Locate and identify every blood parasite.
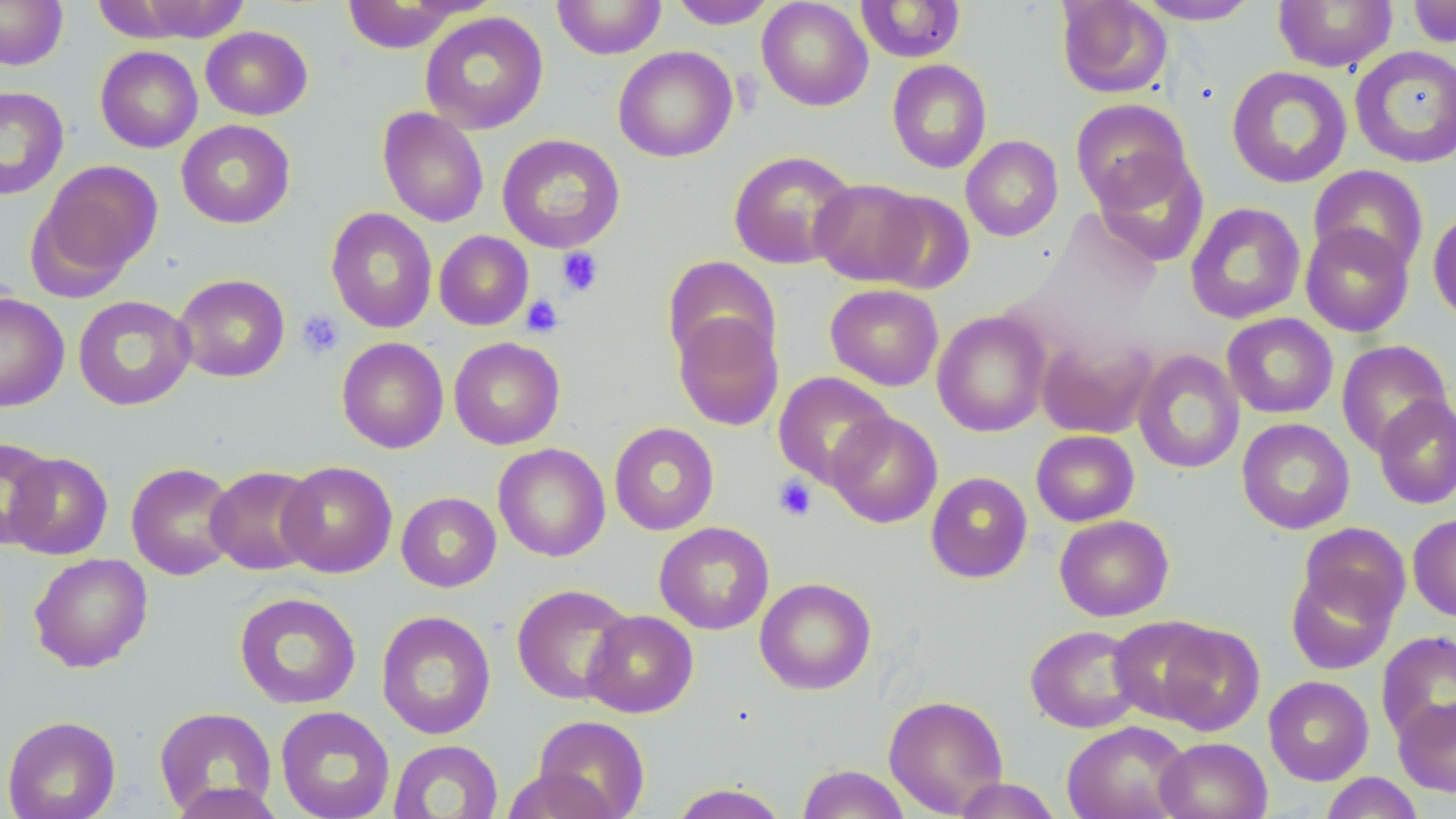
No blood parasites seen.

Summary:
  - Coordinate format: approximate bounding boxes as named x1/y1/x2/y2 corners in pixels
  - Platelet locations: (x1=556, y1=247, x2=604, y2=297), (x1=521, y1=295, x2=564, y2=338), (x1=296, y1=309, x2=345, y2=360), (x1=773, y1=474, x2=818, y2=522)
  - Uninfected red blood cell locations: (x1=0, y1=0, x2=68, y2=70), (x1=552, y1=0, x2=666, y2=59), (x1=756, y1=0, x2=873, y2=111), (x1=1055, y1=0, x2=1172, y2=99), (x1=1133, y1=0, x2=1262, y2=25), (x1=1273, y1=0, x2=1398, y2=73), (x1=121, y1=1, x2=253, y2=42), (x1=342, y1=1, x2=464, y2=53), (x1=669, y1=1, x2=778, y2=29), (x1=855, y1=1, x2=966, y2=62), (x1=1407, y1=1, x2=1456, y2=48), (x1=420, y1=12, x2=549, y2=134), (x1=200, y1=26, x2=313, y2=120), (x1=1350, y1=45, x2=1456, y2=168), (x1=95, y1=46, x2=203, y2=153), (x1=613, y1=46, x2=737, y2=162), (x1=887, y1=59, x2=992, y2=173), (x1=1226, y1=66, x2=1353, y2=188), (x1=0, y1=86, x2=69, y2=199), (x1=1070, y1=97, x2=1192, y2=210), (x1=378, y1=107, x2=489, y2=227), (x1=176, y1=119, x2=295, y2=229), (x1=497, y1=133, x2=625, y2=253), (x1=961, y1=135, x2=1063, y2=241), (x1=728, y1=150, x2=857, y2=269), (x1=1094, y1=151, x2=1209, y2=267), (x1=31, y1=160, x2=164, y2=292), (x1=1309, y1=164, x2=1429, y2=275), (x1=810, y1=178, x2=928, y2=286), (x1=870, y1=190, x2=975, y2=294), (x1=1185, y1=202, x2=1306, y2=324), (x1=325, y1=207, x2=438, y2=334), (x1=1427, y1=207, x2=1456, y2=326), (x1=1300, y1=223, x2=1414, y2=337), (x1=434, y1=231, x2=534, y2=330), (x1=662, y1=256, x2=782, y2=369), (x1=173, y1=274, x2=290, y2=382), (x1=825, y1=284, x2=944, y2=391), (x1=0, y1=293, x2=69, y2=412), (x1=73, y1=295, x2=196, y2=411), (x1=672, y1=310, x2=784, y2=431), (x1=932, y1=310, x2=1051, y2=437), (x1=1222, y1=313, x2=1338, y2=418), (x1=1036, y1=335, x2=1159, y2=439), (x1=336, y1=337, x2=449, y2=454), (x1=449, y1=337, x2=565, y2=450), (x1=1336, y1=340, x2=1453, y2=456), (x1=1133, y1=350, x2=1245, y2=474), (x1=773, y1=371, x2=895, y2=488), (x1=1372, y1=394, x2=1456, y2=509), (x1=826, y1=412, x2=942, y2=528), (x1=1236, y1=417, x2=1355, y2=534), (x1=609, y1=422, x2=720, y2=535), (x1=1031, y1=430, x2=1139, y2=527), (x1=0, y1=436, x2=57, y2=551), (x1=493, y1=443, x2=610, y2=562), (x1=4, y1=452, x2=113, y2=560), (x1=277, y1=460, x2=397, y2=578), (x1=126, y1=462, x2=240, y2=580), (x1=205, y1=465, x2=321, y2=575), (x1=925, y1=471, x2=1032, y2=583), (x1=396, y1=492, x2=501, y2=592), (x1=1408, y1=512, x2=1456, y2=622), (x1=1055, y1=514, x2=1174, y2=621), (x1=654, y1=521, x2=774, y2=635), (x1=1297, y1=522, x2=1411, y2=628), (x1=29, y1=553, x2=153, y2=672), (x1=1285, y1=563, x2=1398, y2=674), (x1=754, y1=577, x2=876, y2=695), (x1=511, y1=583, x2=635, y2=704), (x1=234, y1=592, x2=362, y2=709), (x1=582, y1=609, x2=698, y2=717), (x1=376, y1=610, x2=496, y2=739), (x1=1108, y1=615, x2=1227, y2=724), (x1=1152, y1=622, x2=1265, y2=736), (x1=1025, y1=625, x2=1146, y2=733), (x1=1376, y1=631, x2=1456, y2=746), (x1=1263, y1=675, x2=1374, y2=785), (x1=883, y1=694, x2=1009, y2=817), (x1=1393, y1=696, x2=1456, y2=796), (x1=275, y1=705, x2=395, y2=819), (x1=153, y1=706, x2=277, y2=816), (x1=2, y1=715, x2=121, y2=819), (x1=531, y1=715, x2=651, y2=819), (x1=1061, y1=721, x2=1192, y2=819), (x1=1154, y1=736, x2=1272, y2=819), (x1=388, y1=740, x2=504, y2=819), (x1=797, y1=764, x2=911, y2=819), (x1=501, y1=765, x2=619, y2=819), (x1=1320, y1=772, x2=1424, y2=819), (x1=952, y1=777, x2=1063, y2=818), (x1=164, y1=782, x2=286, y2=819), (x1=669, y1=782, x2=789, y2=819)
  - Slide-level diagnosis: negative for blood parasites
  - Stain: May-Grünwald-Giemsa
  - Modality: optical microscopy
  - Field of view: single
  - Magnification: 1000x
  - Image size: 1456×819 pixels
  - Preparation: thin blood film